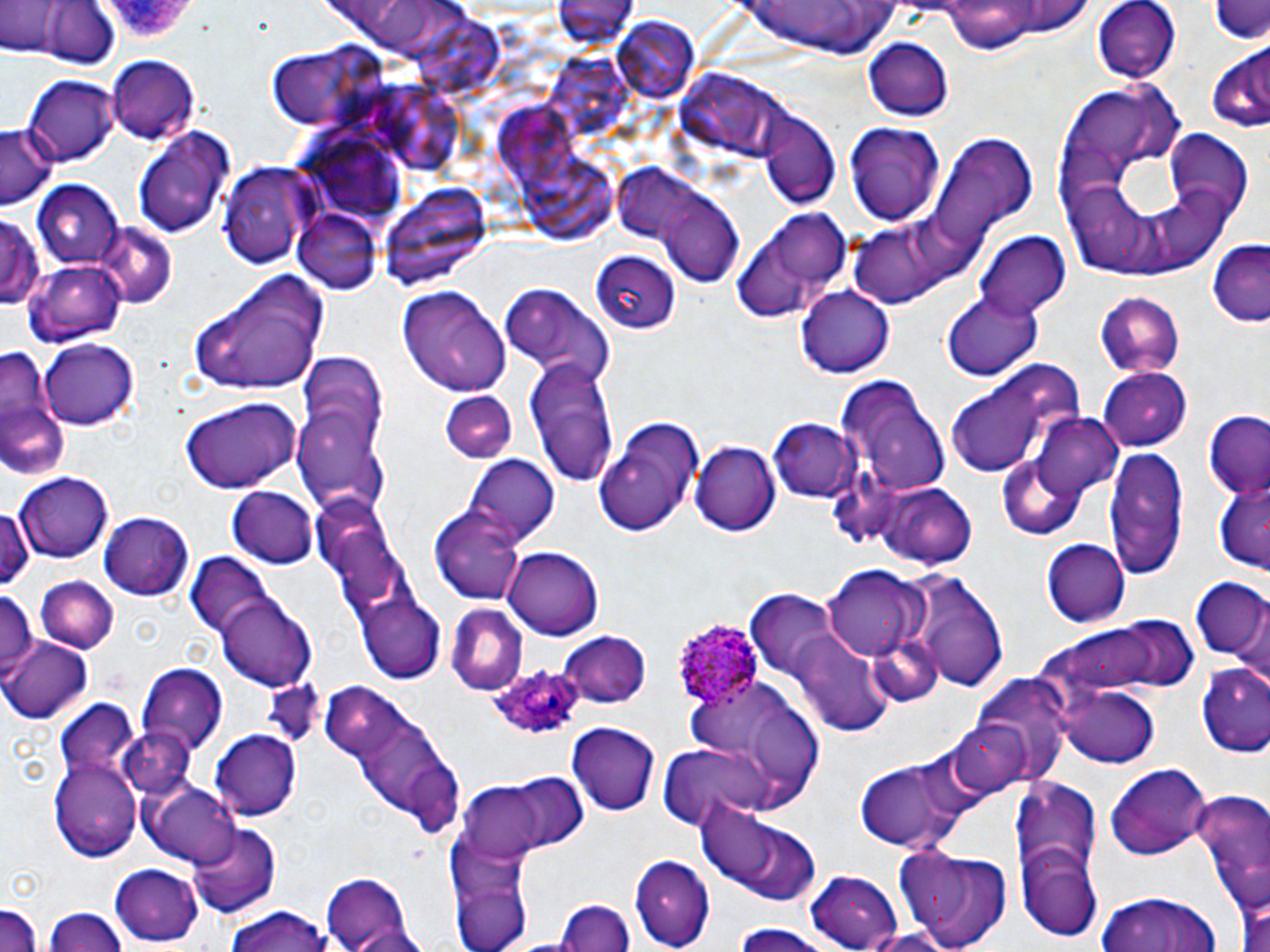

Summary:
  - Coordinate format: approximate bounding boxes as (x1, y1, x2, y2) in pixels
  - Plasmodium ovale-infected red blood cell locations: (666, 617, 761, 710), (485, 660, 583, 741)
  - Uninfected red blood cell locations: (0, 0, 63, 54), (555, 0, 635, 45), (1092, 0, 1180, 82), (938, 1, 1091, 52), (733, 2, 909, 57), (1209, 2, 1269, 44), (29, 3, 120, 70), (407, 15, 518, 102), (609, 18, 705, 105), (863, 39, 954, 121), (262, 46, 381, 130), (1206, 48, 1270, 131), (545, 52, 639, 143), (106, 56, 198, 144), (681, 65, 802, 169), (24, 75, 118, 167), (382, 82, 463, 174), (491, 100, 590, 191), (759, 111, 840, 209), (843, 123, 947, 227), (0, 124, 52, 208), (134, 129, 234, 239), (1164, 132, 1256, 217), (930, 133, 1037, 249), (522, 158, 620, 244), (613, 158, 702, 244), (218, 162, 313, 272), (32, 179, 124, 270), (384, 180, 494, 294), (663, 199, 756, 285), (293, 209, 384, 296), (0, 211, 44, 310), (729, 213, 850, 325), (851, 217, 969, 311), (94, 223, 179, 310), (974, 230, 1071, 321), (1209, 242, 1269, 323), (591, 252, 683, 334), (24, 261, 122, 348), (189, 267, 332, 395), (397, 285, 511, 398), (500, 286, 614, 382), (796, 288, 894, 379), (940, 289, 1043, 382), (1096, 293, 1184, 376), (41, 336, 138, 428), (0, 338, 71, 480), (524, 354, 620, 488), (1097, 368, 1193, 451), (945, 371, 1076, 478), (834, 375, 949, 497), (440, 391, 516, 464), (181, 399, 301, 492), (295, 401, 388, 509), (1201, 412, 1270, 499), (1030, 414, 1125, 504), (770, 417, 860, 501), (690, 440, 781, 537), (1103, 448, 1189, 581), (465, 455, 561, 543), (995, 455, 1088, 539), (16, 472, 116, 561), (1211, 474, 1270, 575), (870, 483, 978, 569), (227, 488, 320, 569), (316, 500, 413, 626), (0, 505, 32, 588), (427, 506, 527, 604), (100, 513, 193, 601), (1042, 538, 1130, 627), (504, 544, 604, 640), (185, 552, 276, 640), (823, 565, 928, 661), (905, 570, 1010, 694), (34, 577, 118, 655), (1190, 578, 1269, 662), (0, 587, 39, 673), (745, 591, 837, 675), (219, 595, 317, 688), (356, 597, 445, 682), (445, 604, 527, 696), (1045, 616, 1184, 696), (790, 629, 892, 735), (557, 630, 654, 708), (2, 638, 93, 723), (1195, 661, 1270, 755), (138, 665, 228, 757), (976, 674, 1075, 786), (684, 677, 822, 807), (1058, 681, 1161, 769), (335, 697, 463, 834), (55, 702, 139, 788), (948, 719, 1035, 799), (567, 720, 661, 814), (116, 728, 192, 807), (210, 730, 303, 818), (655, 743, 769, 828), (50, 754, 143, 861), (855, 754, 971, 855), (1106, 763, 1214, 860), (494, 773, 588, 851), (1012, 774, 1104, 907), (142, 780, 240, 866), (460, 781, 557, 859), (1188, 786, 1270, 908), (697, 803, 820, 904), (185, 822, 278, 916), (445, 830, 535, 952), (895, 846, 1014, 952), (1018, 850, 1100, 941), (630, 853, 715, 950), (109, 863, 205, 944), (805, 869, 904, 952), (1232, 870, 1270, 952), (321, 872, 418, 951), (1095, 889, 1224, 952), (0, 898, 45, 952), (555, 899, 633, 952), (220, 907, 337, 952), (43, 908, 126, 952), (728, 925, 839, 952), (853, 926, 959, 950)
  - Slide-level diagnosis: Plasmodium ovale
  - Modality: optical microscopy
  - Magnification: 1000x
  - Preparation: thin blood smear
  - Field of view: single
  - Stain: May-Grünwald-Giemsa
  - Image size: 1270×952 pixels